Point out each Plasmodium parasite.
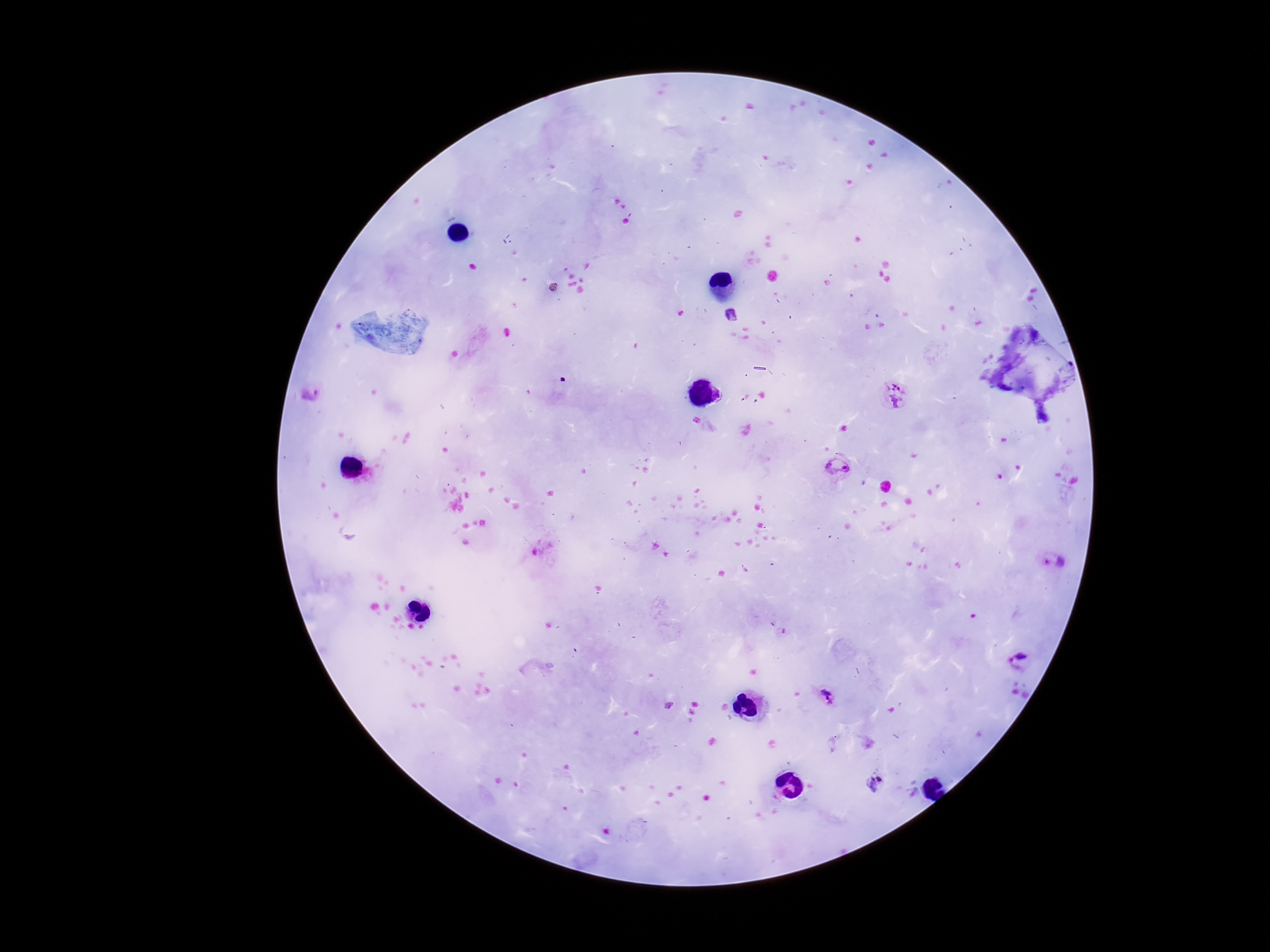
Approximate centers as [x, y] in pixels.
Plasmodium parasites: [730, 315], [312, 394], [894, 395], [838, 467], [1055, 560], [1019, 661], [826, 696], [875, 782].

field_of_view: one from this slide
patient_malaria_status: infected
preparation: thick blood smear
stain: Giemsa
magnification: 100x
image_size: 1270×952 pixels
capture: smartphone camera through the microscope eyepiece